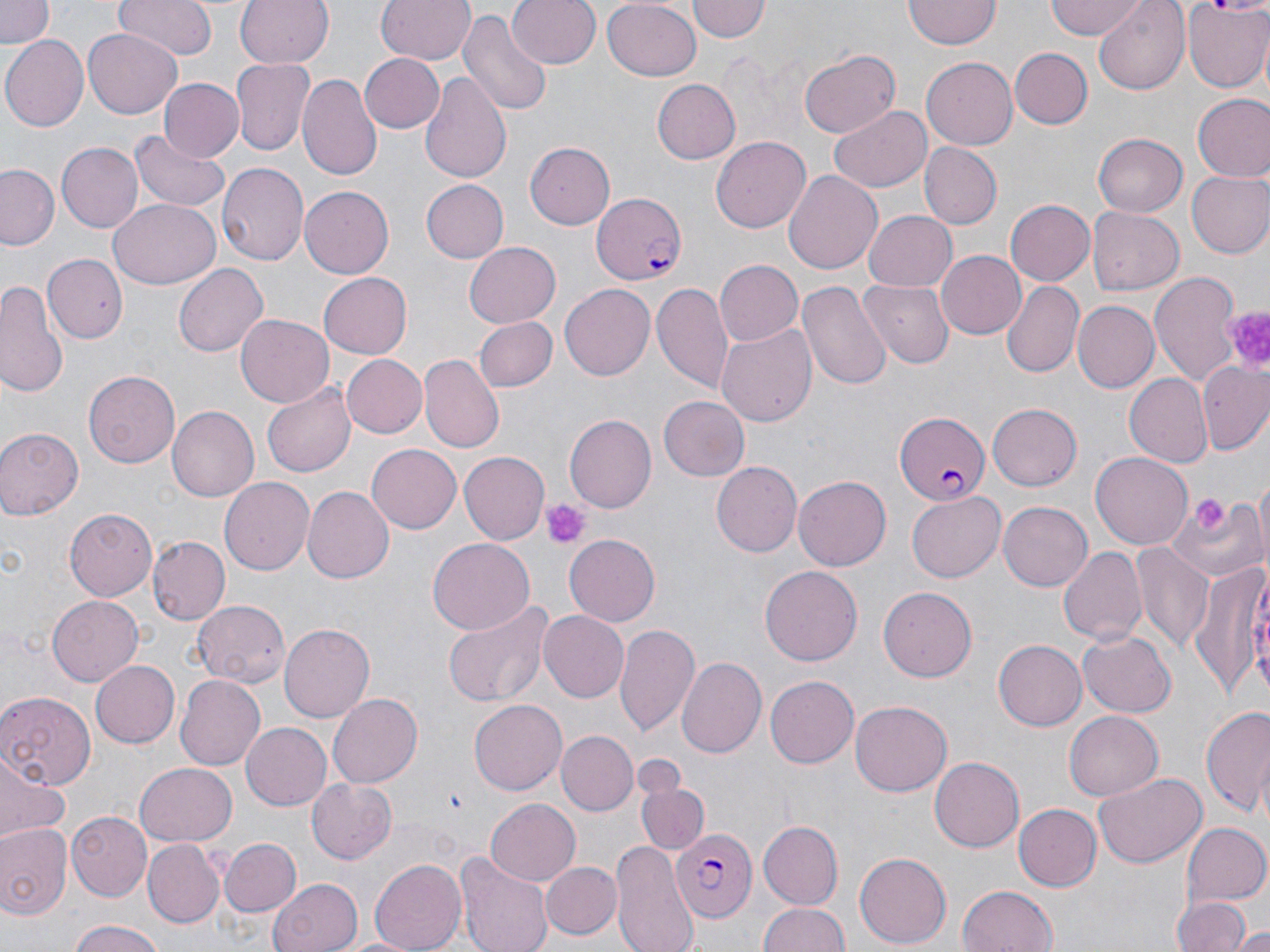
Summary:
  - Coordinate format: approximate bounding boxes as [x1, y1, x2, y2] in pixels
  - Platelet locations: [1220, 305, 1270, 376], [1190, 493, 1230, 536], [541, 497, 594, 549]
  - Uninfected red blood cell locations: [0, 0, 57, 47], [113, 0, 217, 61], [234, 0, 332, 68], [377, 0, 475, 65], [508, 0, 600, 69], [601, 0, 701, 80], [688, 0, 770, 42], [1044, 0, 1151, 40], [1091, 0, 1192, 94], [903, 1, 999, 50], [1182, 1, 1270, 92], [458, 7, 553, 120], [83, 28, 183, 118], [1, 37, 87, 132], [799, 48, 901, 139], [1011, 48, 1092, 128], [360, 55, 443, 134], [923, 57, 1021, 149], [231, 59, 315, 154], [421, 70, 512, 185], [298, 73, 382, 181], [157, 78, 244, 163], [651, 79, 741, 165], [1192, 94, 1270, 184], [828, 104, 932, 191], [128, 130, 231, 216], [1093, 133, 1186, 216], [709, 136, 812, 234], [524, 141, 615, 230], [56, 142, 143, 233], [918, 142, 1001, 230], [215, 164, 308, 269], [1, 165, 61, 249], [783, 169, 883, 275], [1185, 170, 1270, 258], [420, 179, 509, 263], [299, 185, 396, 277], [107, 199, 220, 291], [1006, 199, 1095, 286], [1087, 206, 1184, 294], [863, 210, 957, 293], [463, 242, 561, 329], [934, 249, 1027, 340], [44, 255, 127, 345], [714, 260, 802, 346], [172, 262, 268, 356], [319, 272, 413, 358], [1151, 272, 1245, 389], [860, 279, 954, 370], [0, 281, 69, 397], [797, 281, 892, 390], [1000, 281, 1083, 378], [559, 282, 655, 377], [650, 282, 734, 395], [1072, 301, 1158, 392], [234, 315, 334, 407], [474, 317, 557, 392], [716, 321, 815, 427], [342, 354, 427, 438], [421, 355, 505, 453], [1197, 360, 1269, 457], [84, 369, 181, 468], [1124, 374, 1212, 468], [263, 384, 355, 478], [659, 396, 750, 480], [987, 404, 1082, 489], [167, 407, 259, 502], [563, 415, 656, 513], [0, 428, 81, 520], [367, 444, 461, 534], [458, 452, 548, 544], [1091, 452, 1194, 550], [710, 461, 800, 556], [794, 476, 891, 569], [220, 478, 314, 575], [303, 486, 395, 584], [907, 493, 1004, 582], [1166, 494, 1264, 584], [998, 500, 1095, 591], [63, 509, 159, 600], [564, 534, 660, 626], [145, 535, 228, 624], [427, 538, 534, 633], [1058, 545, 1145, 648], [1131, 545, 1212, 651], [1190, 556, 1270, 707], [761, 566, 861, 664], [879, 586, 978, 681], [46, 594, 141, 687], [193, 600, 290, 687], [443, 600, 557, 708], [538, 611, 628, 702], [280, 622, 374, 721], [616, 623, 702, 738], [1078, 631, 1178, 717], [994, 638, 1087, 731], [676, 656, 767, 760], [90, 659, 180, 747], [174, 674, 265, 770], [765, 675, 859, 767], [0, 689, 97, 789], [326, 694, 422, 788], [469, 700, 567, 795], [850, 700, 953, 797], [1200, 701, 1270, 820], [1064, 710, 1162, 801], [240, 720, 332, 810], [555, 731, 638, 816], [929, 757, 1023, 853], [0, 759, 69, 845], [134, 764, 236, 847], [1094, 771, 1205, 870], [306, 778, 397, 865], [638, 778, 706, 854], [485, 799, 580, 886], [1013, 804, 1100, 892], [66, 812, 154, 900], [757, 821, 843, 910], [1183, 823, 1270, 907], [0, 824, 70, 920], [220, 838, 302, 917], [610, 838, 700, 952], [143, 839, 224, 928], [454, 850, 552, 952], [854, 852, 950, 948], [370, 859, 465, 951], [540, 861, 622, 940], [268, 876, 360, 952], [958, 883, 1058, 952], [1173, 896, 1252, 952], [757, 901, 850, 951], [66, 923, 170, 952], [1234, 926, 1270, 952]
  - Plasmodium falciparum-infected red blood cell locations: [590, 193, 689, 285], [895, 410, 990, 504], [674, 823, 758, 923]
  - Slide-level diagnosis: Plasmodium falciparum
  - Field of view: one of a larger specimen
  - Magnification: 1000x
  - Stain: May-Grünwald-Giemsa
  - Modality: light microscopy
  - Preparation: thin blood smear
  - Image size: 1270×952 pixels